Assess the morphology of the red blood cells.
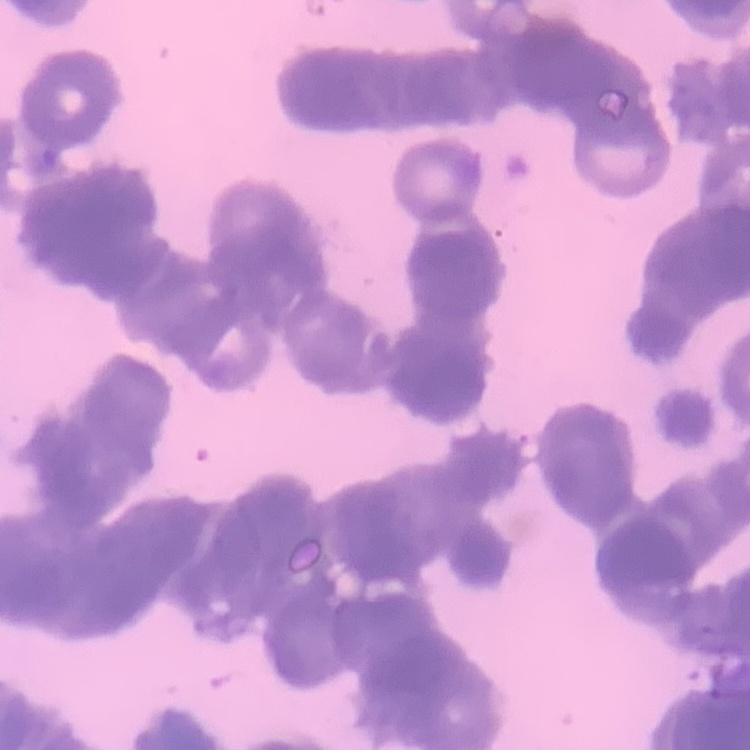
Rouleaux formation.

Summary:
  - Preparation: thin peripheral smear
  - Image type: one tile cut from a larger photomicrograph
  - Stain: Field's or Giemsa